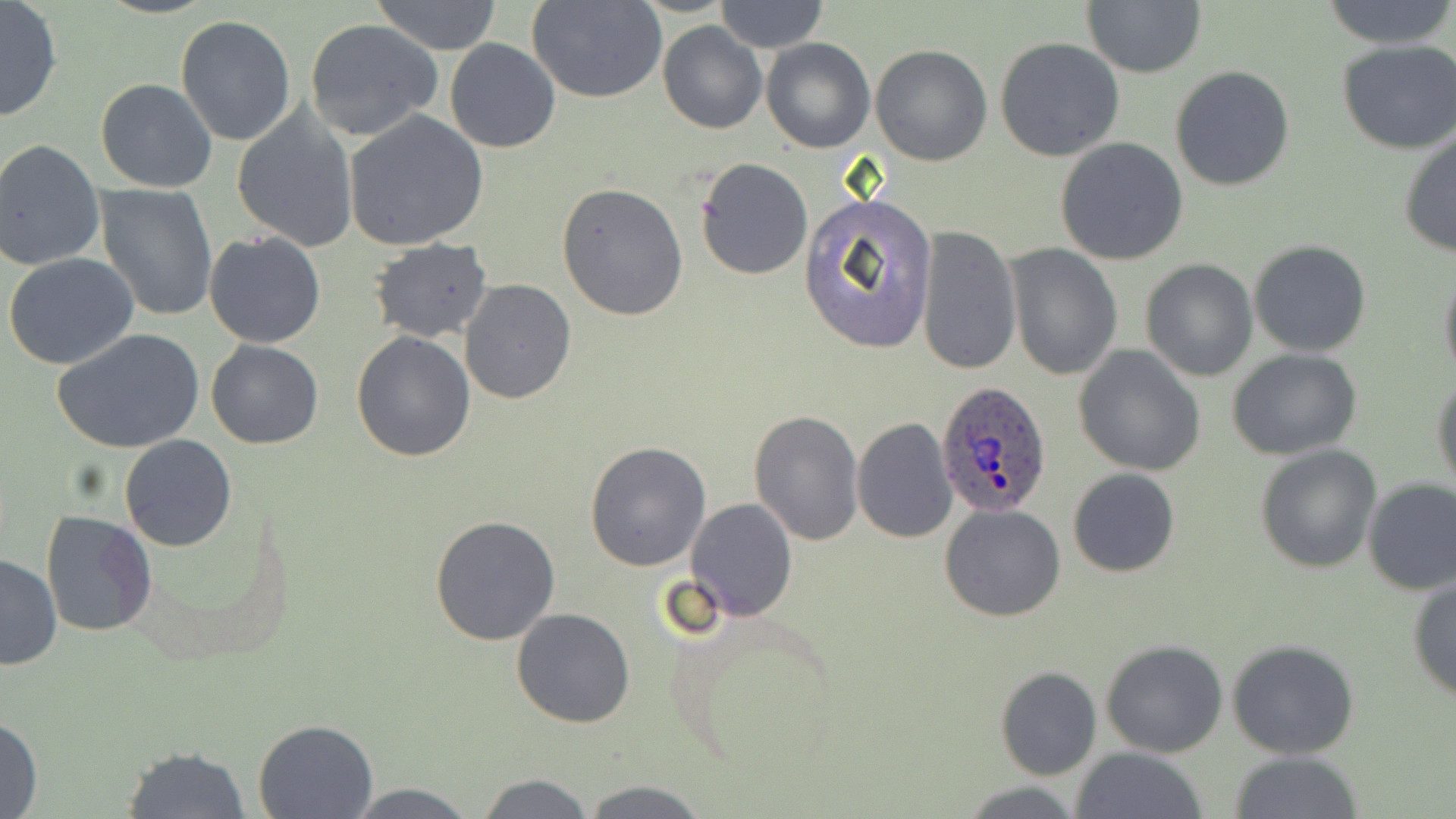
Approximate bounding boxes as named x1/y1/x2/y2 corners in pixels. Plasmodium ovale-infected red blood cell locations: (x1=935, y1=383, x2=1052, y2=517). Uninfected red blood cell locations: (x1=369, y1=0, x2=504, y2=54), (x1=530, y1=0, x2=667, y2=104), (x1=715, y1=0, x2=827, y2=53), (x1=1322, y1=0, x2=1456, y2=51), (x1=0, y1=1, x2=63, y2=123), (x1=1083, y1=2, x2=1206, y2=78), (x1=176, y1=16, x2=296, y2=146), (x1=303, y1=18, x2=443, y2=141), (x1=658, y1=22, x2=767, y2=135), (x1=995, y1=37, x2=1125, y2=161), (x1=444, y1=38, x2=561, y2=153), (x1=761, y1=38, x2=874, y2=153), (x1=1337, y1=40, x2=1456, y2=153), (x1=870, y1=44, x2=994, y2=167), (x1=1171, y1=65, x2=1294, y2=191), (x1=95, y1=79, x2=217, y2=192), (x1=232, y1=109, x2=359, y2=251), (x1=345, y1=110, x2=489, y2=251), (x1=1398, y1=130, x2=1456, y2=258), (x1=1055, y1=138, x2=1189, y2=265), (x1=0, y1=140, x2=105, y2=271), (x1=694, y1=156, x2=813, y2=280), (x1=557, y1=182, x2=689, y2=323), (x1=95, y1=185, x2=217, y2=321), (x1=801, y1=193, x2=938, y2=351), (x1=917, y1=225, x2=1021, y2=376), (x1=205, y1=231, x2=325, y2=348), (x1=368, y1=238, x2=493, y2=343), (x1=1248, y1=239, x2=1373, y2=357), (x1=1006, y1=243, x2=1122, y2=381), (x1=4, y1=254, x2=140, y2=371), (x1=1140, y1=258, x2=1258, y2=382), (x1=1438, y1=265, x2=1456, y2=383), (x1=460, y1=280, x2=576, y2=405), (x1=51, y1=328, x2=205, y2=453), (x1=351, y1=331, x2=475, y2=462), (x1=206, y1=341, x2=324, y2=449), (x1=1071, y1=344, x2=1207, y2=477), (x1=1228, y1=349, x2=1362, y2=459), (x1=1431, y1=373, x2=1456, y2=492), (x1=751, y1=409, x2=864, y2=544), (x1=851, y1=416, x2=958, y2=542), (x1=119, y1=435, x2=236, y2=552), (x1=585, y1=442, x2=712, y2=570), (x1=1254, y1=444, x2=1381, y2=572), (x1=1068, y1=467, x2=1181, y2=578), (x1=1362, y1=477, x2=1456, y2=595), (x1=685, y1=497, x2=798, y2=620), (x1=940, y1=503, x2=1067, y2=622), (x1=39, y1=510, x2=158, y2=637), (x1=430, y1=514, x2=561, y2=647), (x1=1, y1=554, x2=63, y2=670), (x1=1408, y1=578, x2=1456, y2=702), (x1=512, y1=609, x2=635, y2=729), (x1=1099, y1=638, x2=1228, y2=758), (x1=1227, y1=639, x2=1359, y2=759), (x1=995, y1=666, x2=1102, y2=780), (x1=0, y1=712, x2=43, y2=819), (x1=252, y1=718, x2=378, y2=819), (x1=118, y1=744, x2=253, y2=818), (x1=1072, y1=746, x2=1208, y2=819), (x1=1228, y1=751, x2=1364, y2=819), (x1=473, y1=772, x2=596, y2=817), (x1=580, y1=780, x2=709, y2=818), (x1=958, y1=780, x2=1084, y2=817), (x1=343, y1=783, x2=480, y2=817). Slide-level diagnosis: Plasmodium ovale. Captured at 1000x magnification. Thin blood film. Image is 1456×819 pixels. May-Grünwald-Giemsa-stained preparation. One field of a larger specimen. Light microscopy.